Classify this cell by malaria status.
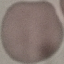

It is uninfected.

Summary:
  - Capture: smartphone camera at the microscope eyepiece
  - Image type: automatically extracted cell patch, resized to 64 × 64 pixels
  - Preparation: thin blood film
  - Stain: Giemsa